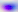

Micrograph. Toxoplasma gondii is seen. Captured at 400x magnification.